Classify this cell by malaria status.
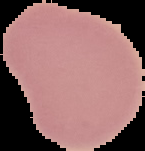

Uninfected.

From a thin blood film. Image is 145×151 pixels. Segmented cell region on a black background.